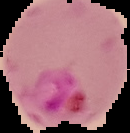 From a thin blood smear. Image is 130×133 pixels. Malaria status: parasitized. The area outside the segmented cell region is set to black.